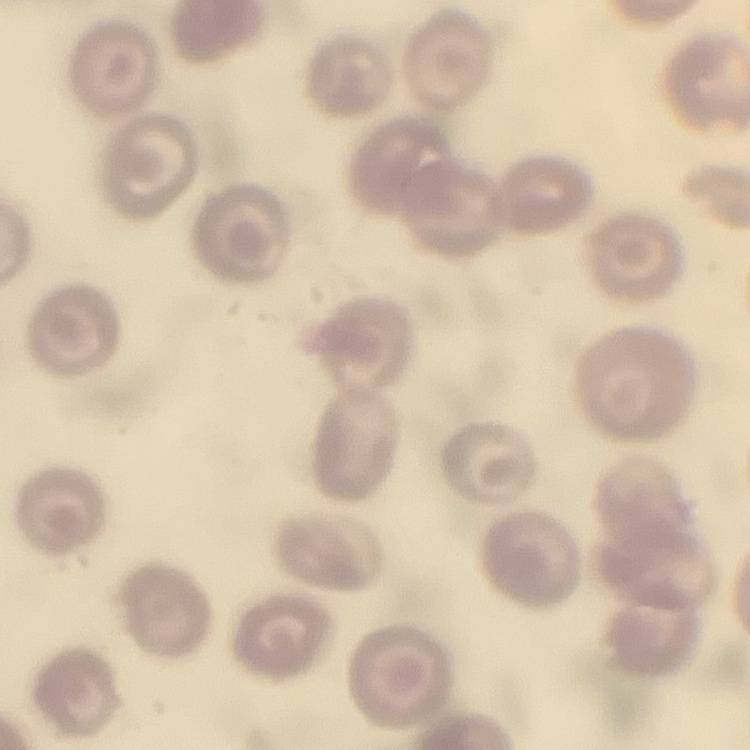

Summary:
  - Red blood cell morphology: no rouleaux formation
  - Preparation: thin peripheral smear
  - Stain: Field's or Giemsa
  - Image type: square crop of a larger photomicrograph